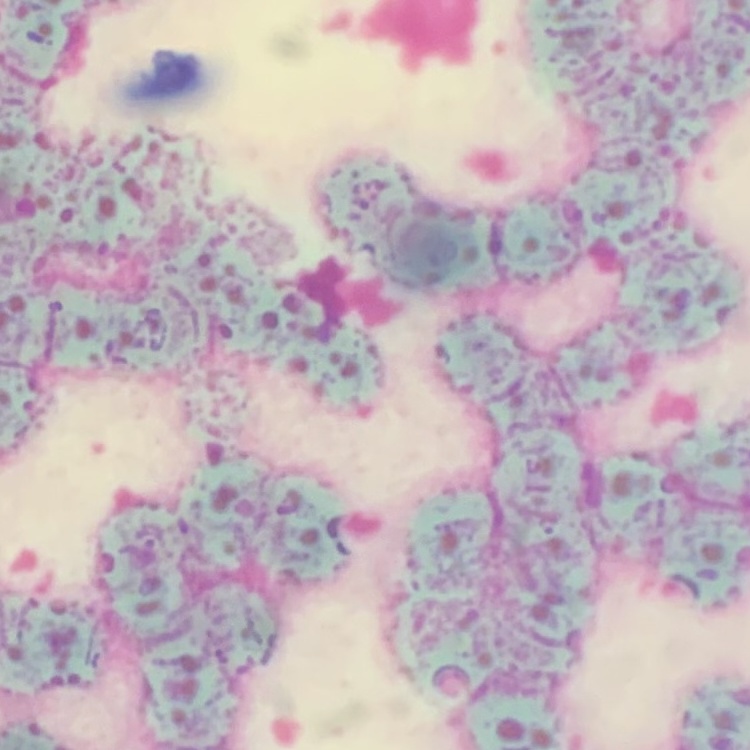

The erythrocytes show rouleaux formation. One tile cut from a larger photomicrograph. Thin blood film. Field's or Giemsa stain.